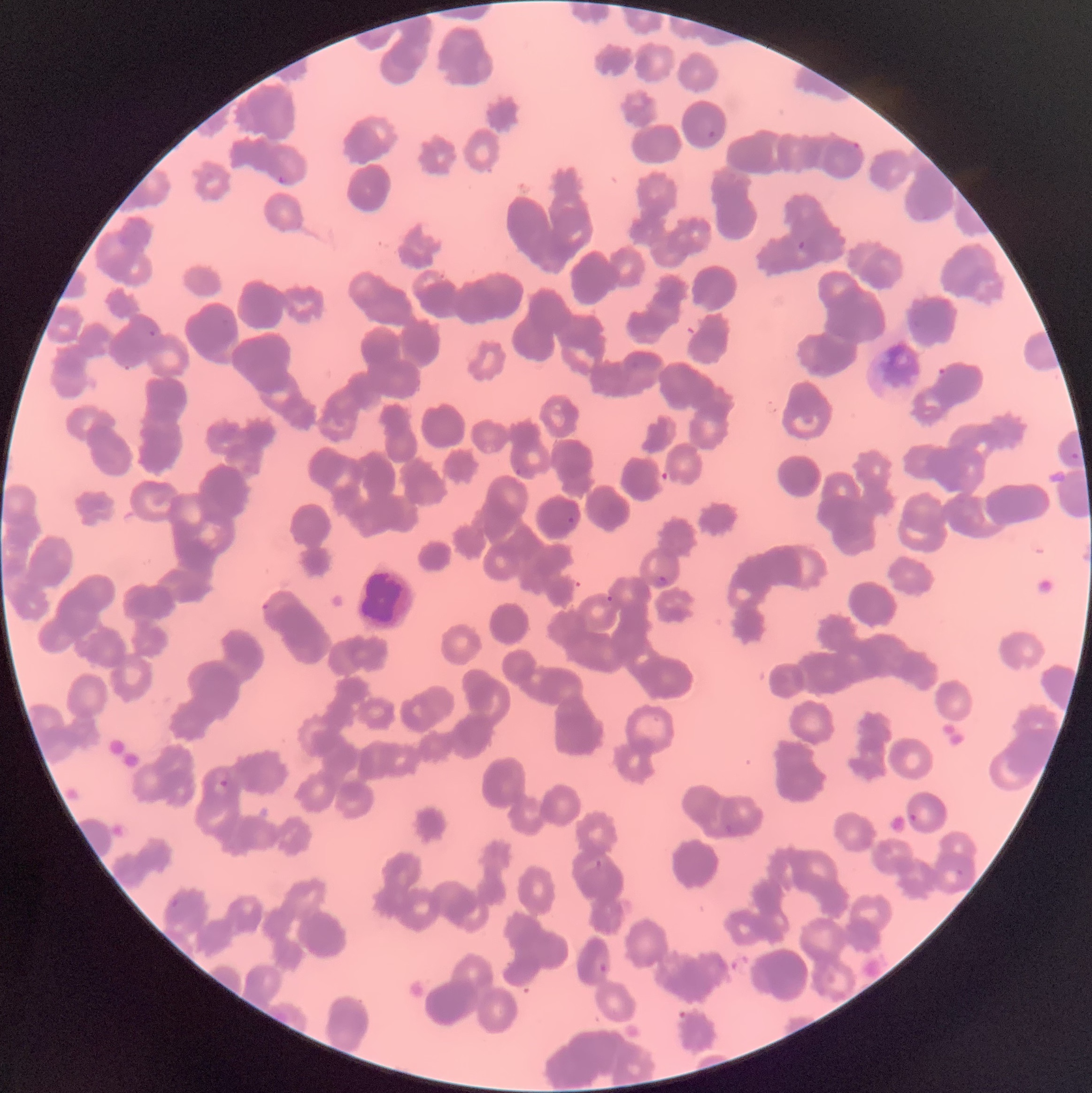

Summary:
  - Coordinate format: approximate bounding boxes as (x1,y1)-(x2,y2) corner pairs in pixels
  - Plasmodium parasite locations: (708,130)-(716,138), (848,139)-(861,152), (278,173)-(287,186), (797,240)-(807,251), (147,329)-(157,338), (938,366)-(952,380), (1070,452)-(1080,463), (515,466)-(523,477), (565,515)-(575,524), (654,575)-(669,590), (605,593)-(615,604), (260,601)-(273,613), (218,779)-(228,788), (909,812)-(918,824), (722,822)-(735,837), (595,858)-(605,872), (954,868)-(964,878), (169,897)-(180,910), (597,962)-(608,974)
  - Preparation: thin blood film
  - Red blood cell morphology: rouleaux formation
  - Image size: 1092×1093 pixels
  - Modality: optical microscopy